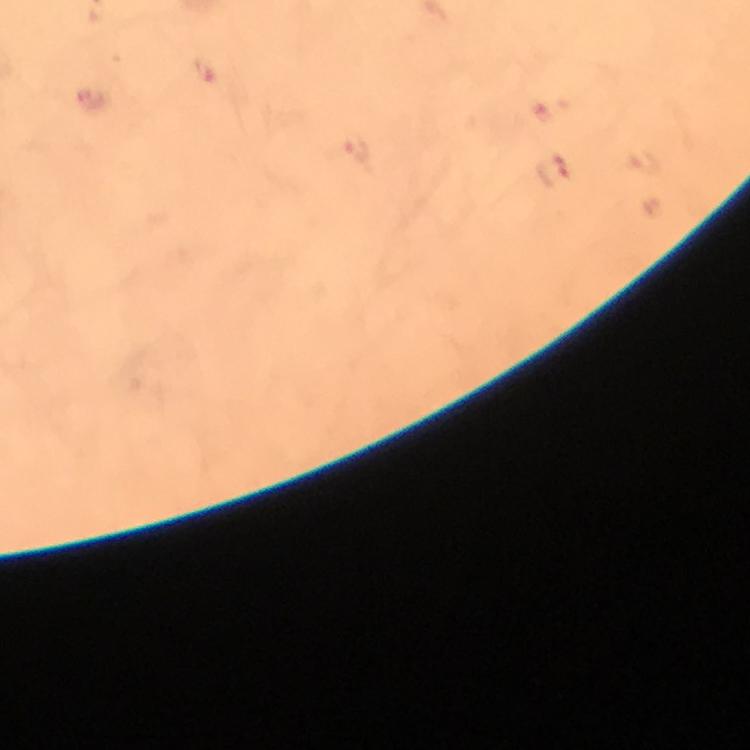

preparation = thick blood film
immersion oil = used
context = from a malaria diagnostic workup
cropped from = a single field of view
magnification = 100x
malaria parasite locations = approximate centers as {x, y} in pixels: {206, 70}, {356, 146}, {553, 169}
image size = 750×750 pixels
stain = Giemsa
capture = smartphone photograph through a microscope